Outline each Plasmodium falciparum-infected red blood cell.
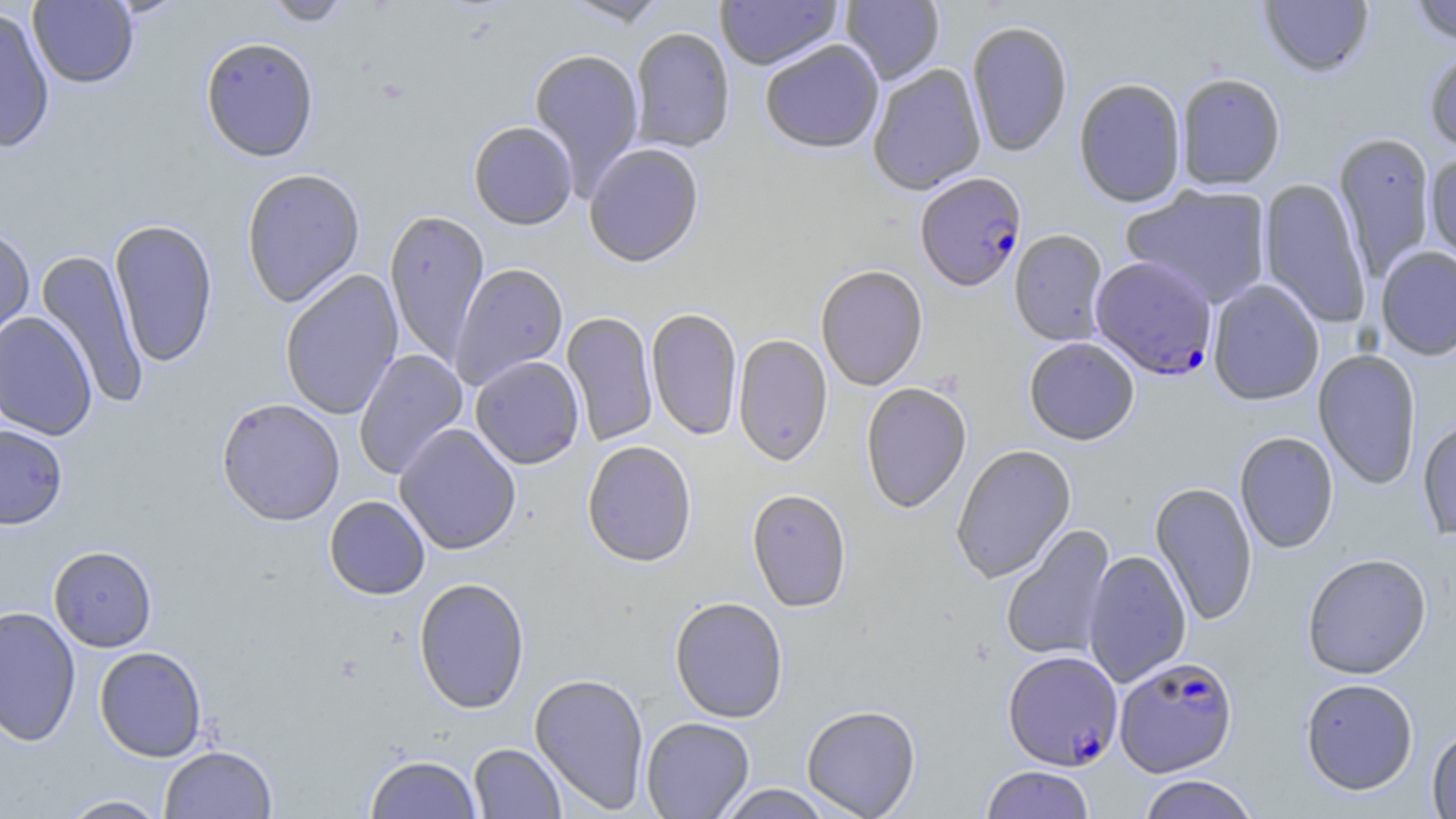

Approximate bounding boxes as (x1,y1)-(x2,y2) corner pairs in pixels.
Plasmodium falciparum-infected red blood cells: (915,172)-(1027,291), (1090,255)-(1218,380), (1003,650)-(1122,770), (1114,655)-(1238,777).

Uninfected red blood cell locations: (27,0)-(139,89), (263,0)-(352,27), (562,0)-(670,27), (715,0)-(842,70), (840,0)-(945,84), (1258,0)-(1374,77), (1408,0)-(1456,45), (0,8)-(55,153), (966,20)-(1073,157), (630,27)-(735,153), (200,36)-(320,162), (760,39)-(884,154), (1423,44)-(1456,157), (529,47)-(644,197), (867,63)-(986,195), (1175,71)-(1286,190), (1073,78)-(1186,208), (468,121)-(578,230), (1333,131)-(1436,282), (584,142)-(704,267), (1425,151)-(1456,271), (241,167)-(366,308), (1259,177)-(1372,329), (1120,184)-(1272,309), (385,209)-(489,366), (109,218)-(218,368), (0,224)-(35,347), (1009,229)-(1109,346), (1376,246)-(1456,360), (36,248)-(149,411), (450,263)-(569,390), (815,265)-(928,390), (280,269)-(404,420), (1207,279)-(1324,405), (646,308)-(743,440), (562,311)-(658,446), (0,312)-(97,440), (733,334)-(833,466), (1024,337)-(1140,445), (353,348)-(468,480), (1313,349)-(1422,490), (470,355)-(584,469), (861,382)-(972,514), (216,397)-(346,526), (1417,416)-(1456,543), (395,423)-(522,554), (0,424)-(68,529), (1234,431)-(1338,554), (582,440)-(697,567), (951,444)-(1076,583), (1150,481)-(1258,627), (747,489)-(852,612), (324,496)-(430,599), (1001,524)-(1116,663), (48,545)-(158,652), (1083,549)-(1192,687), (1302,553)-(1432,679), (413,577)-(530,714), (669,596)-(788,723), (0,606)-(81,746), (94,646)-(207,762), (529,672)-(650,813), (1300,677)-(1419,795), (801,704)-(921,818), (640,716)-(755,818), (1426,724)-(1456,819), (468,743)-(565,818), (159,744)-(278,819), (364,753)-(483,818), (980,766)-(1095,818), (1135,775)-(1260,819), (714,784)-(838,818), (58,794)-(170,818). Slide-level diagnosis: Plasmodium falciparum. May-Grünwald-Giemsa-stained preparation. Image is 1456×819 pixels. Thin blood film. Single field of view. 1000x magnification. Light microscopy.